Assess the morphology of the red blood cells.
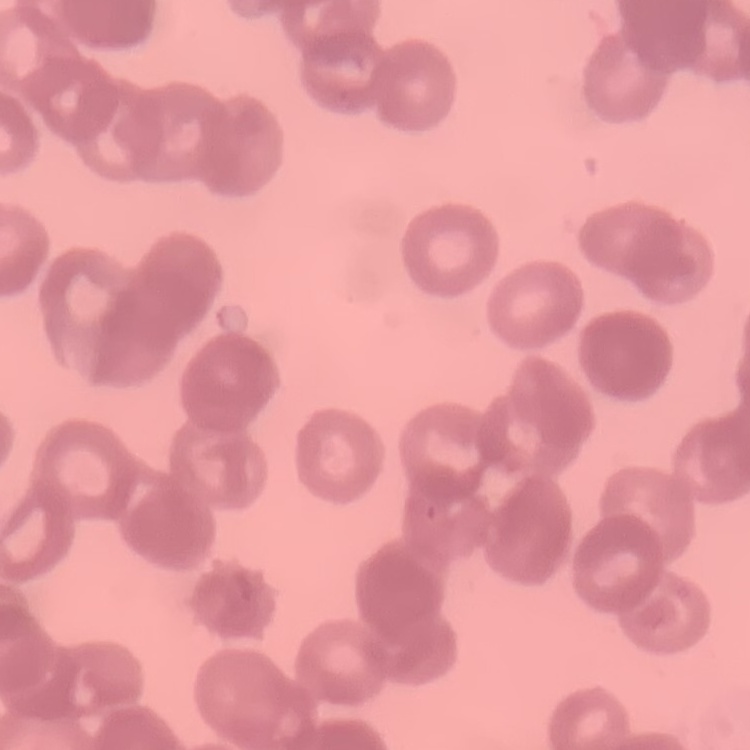
Rouleaux formation.

Summary:
  - Image type: square crop of a larger photomicrograph
  - Preparation: thin peripheral smear
  - Stain: Field's or Giemsa